Locate every blood parasite and identify its species.
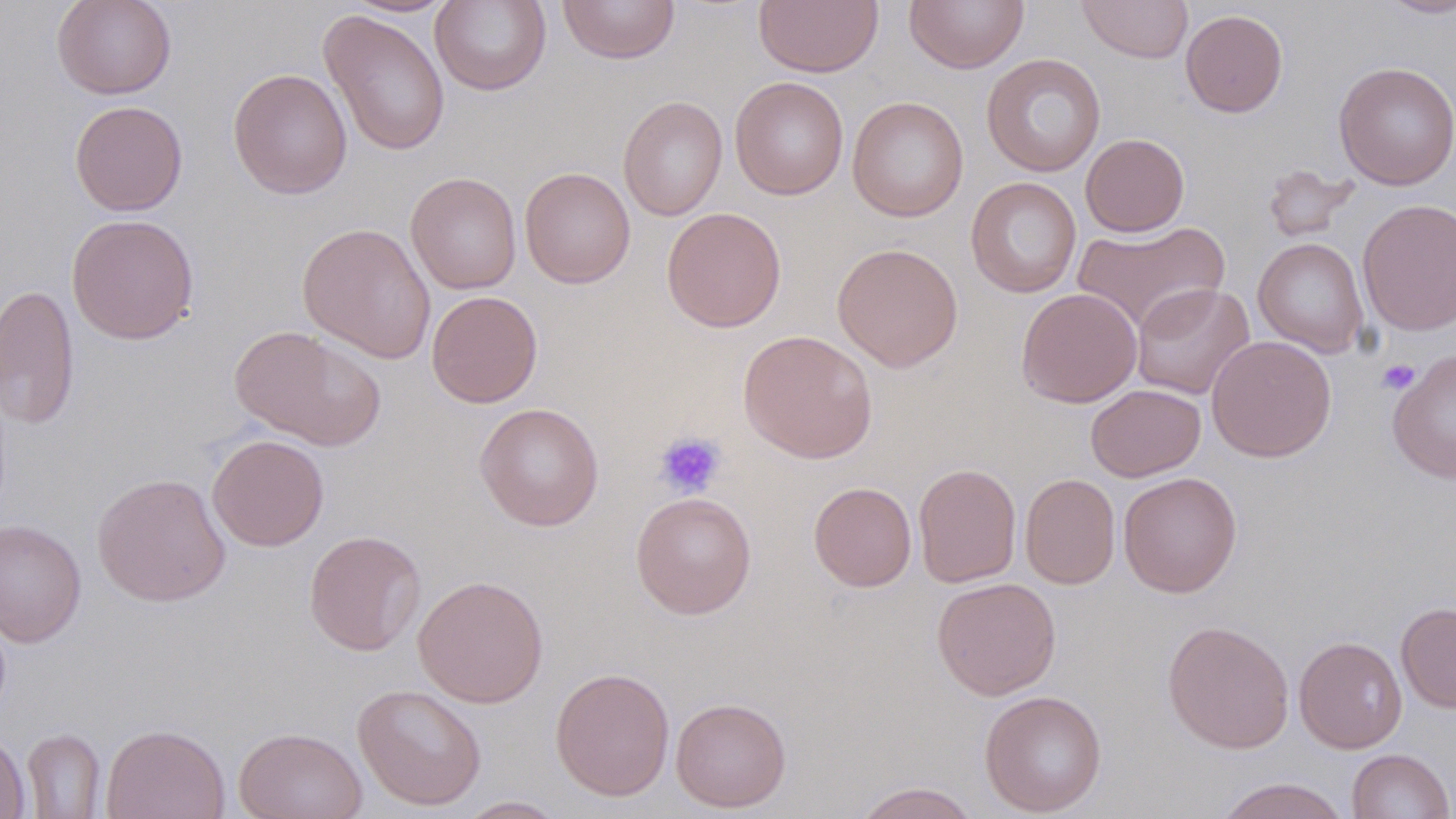

No blood parasites seen.

Approximate bounding boxes as (x1,y1)-(x2,y2) corner pairs in pixels. Uninfected red blood cell locations: (51,0)-(177,100), (430,0)-(551,96), (557,0)-(681,64), (754,0)-(883,77), (904,0)-(1029,73), (1077,0)-(1193,63), (1378,0)-(1455,19), (345,1)-(456,17), (319,9)-(451,157), (1180,9)-(1288,117), (981,53)-(1107,177), (1333,61)-(1456,190), (228,68)-(353,199), (729,76)-(849,200), (618,95)-(728,221), (847,96)-(968,221), (69,100)-(188,216), (1080,133)-(1190,237), (1261,163)-(1360,243), (519,167)-(636,289), (406,171)-(521,295), (965,177)-(1082,298), (1357,198)-(1456,336), (661,207)-(786,332), (66,213)-(200,345), (1071,219)-(1230,335), (297,222)-(436,363), (1253,237)-(1370,357), (831,242)-(964,371), (1131,282)-(1255,400), (0,283)-(80,431), (1016,287)-(1142,408), (427,290)-(543,408), (230,325)-(386,452), (737,330)-(878,463), (1207,334)-(1337,463), (1388,347)-(1456,484), (1085,384)-(1206,482), (475,402)-(604,531), (206,434)-(329,551), (913,463)-(1022,587), (1117,472)-(1243,598), (92,473)-(231,607), (1020,473)-(1120,589), (809,482)-(917,591), (630,491)-(757,618), (0,519)-(87,648), (304,530)-(426,656), (413,574)-(548,708), (931,577)-(1061,700), (1396,601)-(1456,712), (1162,620)-(1295,753), (1293,635)-(1408,753), (550,666)-(675,801), (352,683)-(487,811), (979,690)-(1108,817), (670,696)-(791,813), (100,723)-(231,819), (234,727)-(368,819), (21,728)-(106,818), (0,730)-(30,819), (1346,748)-(1454,818), (1215,777)-(1351,819), (851,781)-(981,819), (454,796)-(569,818). Platelet locations: (1377,358)-(1421,395), (654,430)-(727,498). Slide-level diagnosis: negative for blood parasites. May-Grünwald-Giemsa-stained preparation. Single field of view. Optical microscopy. Thin blood smear. Image is 1456×819 pixels. 1000x magnification.